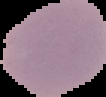
From a thin blood smear. Image is 106×97 pixels. The area outside the segmented cell region is set to black. Result: negative for malaria parasites.